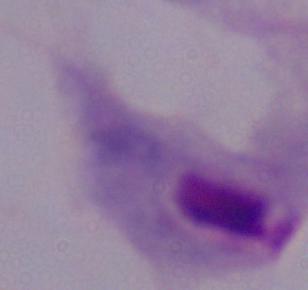
Summary:
  - Modality: micrograph
  - Magnification: 1000x
  - Identification: trichomonad